Identify the parasite.
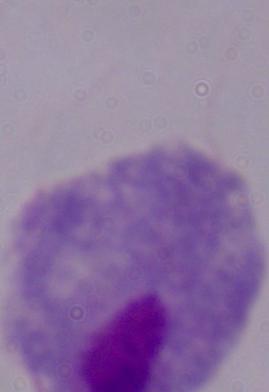
A trichomonad.

Photomicrograph. 1000x magnification.